Describe the morphology of the red blood cells.
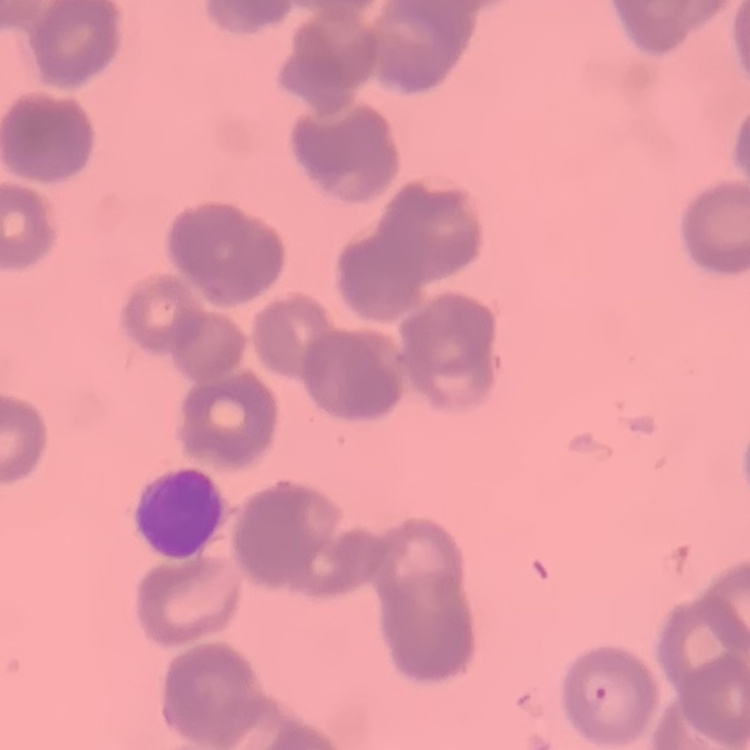
They show rouleaux formation.

Stained with either Field's or Giemsa. Thin blood film. One tile cut from a larger photomicrograph.